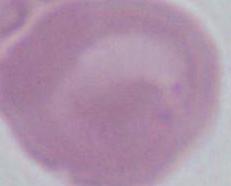

modality = photomicrograph
magnification = 1000x
identification = red blood cell